Give the position of every leukocyte visible.
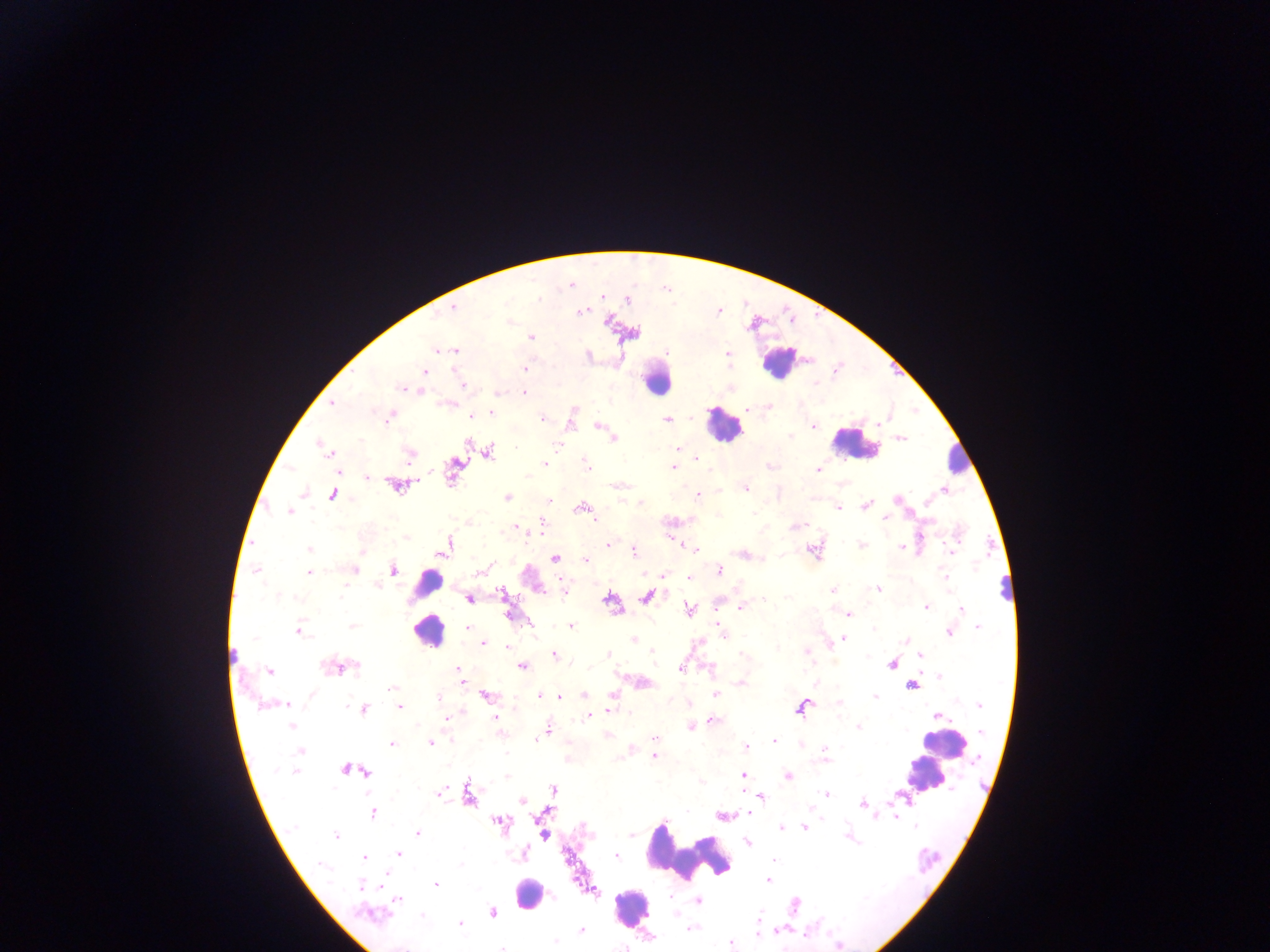

Approximate centers as (x, y) in pixels.
Leukocytes: (779, 360), (655, 378), (724, 425), (854, 442), (958, 460), (427, 583), (428, 630), (943, 744), (926, 774), (689, 852), (529, 894), (630, 907).

{
  "country": "Ghana",
  "image_size": "1270×952 pixels",
  "preparation": "thick blood film",
  "plasmodium_parasite_locations": "approximate centers as (x, y) in pixels: (571, 283), (628, 299), (452, 308), (581, 311), (509, 322), (531, 337), (437, 350), (456, 351), (727, 352), (524, 367), (423, 371), (462, 384), (418, 390), (497, 392), (524, 393), (331, 403), (446, 403), (749, 408), (491, 412), (390, 416), (471, 416), (542, 418), (570, 418), (667, 419), (599, 424), (813, 425), (900, 437), (613, 439), (322, 445), (677, 449), (487, 451), (329, 453), (409, 455), (695, 457), (543, 464), (587, 465), (455, 466), (673, 467), (818, 470), (368, 478), (396, 485), (619, 485), (745, 487), (945, 489), (303, 492), (332, 494), (697, 496), (507, 497), (897, 499), (547, 502), (865, 505), (581, 507), (837, 507), (288, 511), (884, 520), (540, 526), (795, 526), (514, 527), (862, 544), (608, 545), (445, 547), (901, 547), (694, 549), (309, 550), (633, 550), (813, 550), (743, 554), (555, 558), (585, 559), (256, 569), (352, 569), (392, 569), (483, 569), (718, 571), (308, 573), (689, 576), (563, 588), (878, 589), (833, 591), (502, 594), (647, 596), (469, 598), (763, 598), (610, 600), (926, 606), (742, 607), (961, 609), (690, 610), (507, 614), (847, 614), (529, 622), (719, 623), (570, 625), (978, 626), (467, 628), (296, 630), (949, 631), (846, 634), (724, 637), (634, 638), (845, 639), (483, 643), (506, 647), (806, 652), (607, 654), (919, 654), (553, 655), (892, 662), (522, 665), (339, 667), (458, 669), (680, 669), (270, 670), (938, 677), (740, 682), (911, 684), (391, 685), (875, 694), (539, 695), (583, 695), (613, 695), (715, 695), (485, 696), (560, 696), (286, 703), (837, 703), (980, 705), (400, 707), (801, 707), (363, 709), (609, 710), (938, 715), (446, 717), (588, 717), (495, 718), (712, 719), (291, 726), (691, 726), (858, 726), (548, 729), (607, 734), (654, 738), (535, 740), (772, 740), (430, 742), (392, 743), (745, 748), (300, 750), (631, 750), (824, 754), (653, 756), (566, 757), (347, 770), (364, 770), (296, 771), (742, 776), (787, 776), (701, 781), (553, 789), (439, 793), (467, 794), (827, 794), (760, 796), (522, 800), (863, 804), (372, 812), (748, 812), (894, 813), (540, 815), (722, 815), (499, 821), (804, 827), (781, 828), (418, 833), (543, 835), (335, 836), (630, 836), (848, 836), (747, 843), (398, 853), (523, 855), (615, 855), (363, 858), (772, 860), (768, 880), (380, 883), (435, 884), (362, 886), (590, 890), (397, 899), (697, 900), (492, 913), (373, 914), (460, 925), (776, 929), (580, 931), (757, 932), (554, 941), (730, 943), (503, 946)",
  "field_of_view": "single",
  "capture": "mobile-phone photograph through a microscope"
}